Give the position of each P. falciparum parasite with its life-cycle stage, each leukocyte, and any debris.
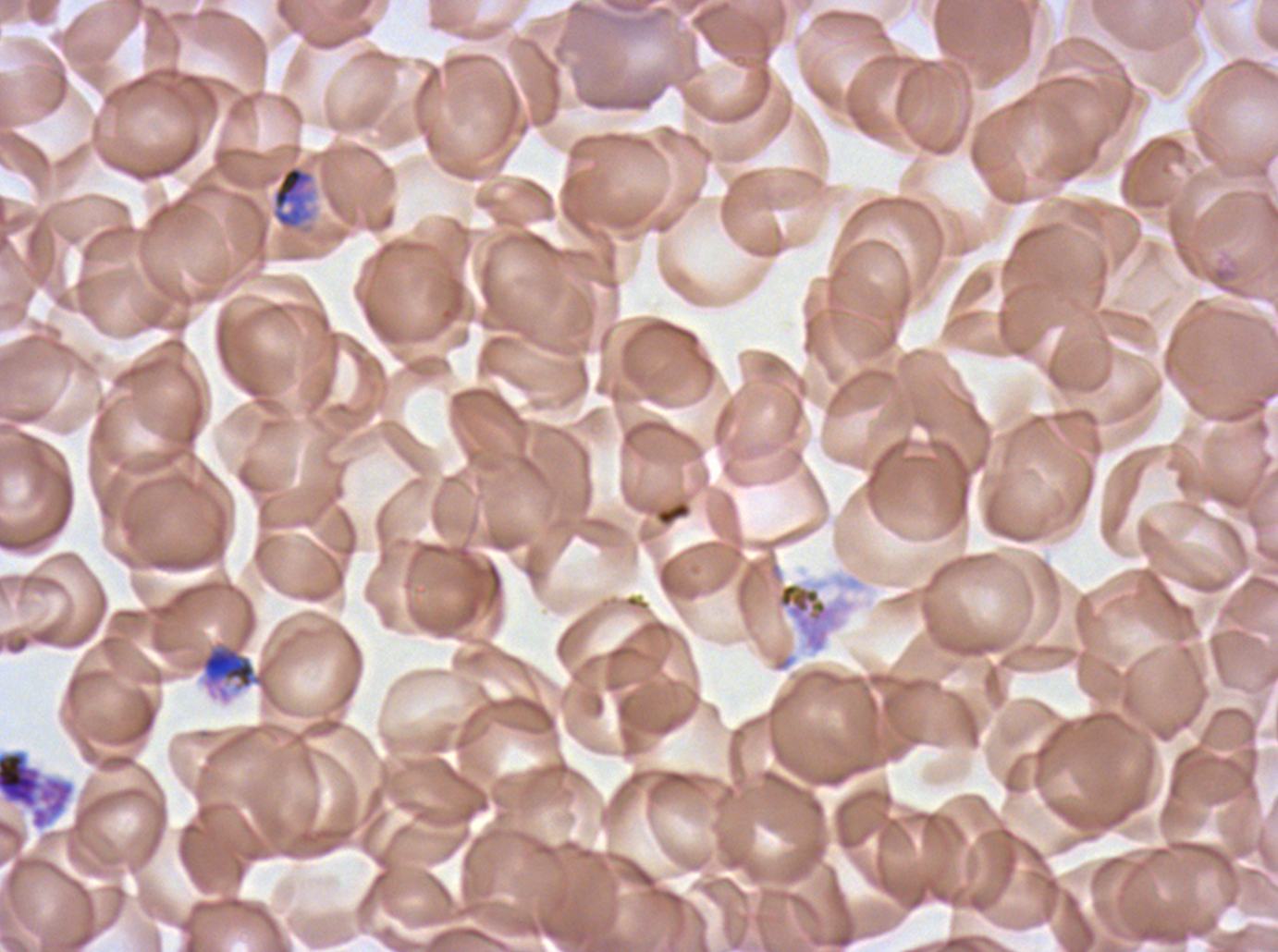

Approximate bounding boxes as [x1, y1, x2, y2] in pixels.
Late trophozoites: [270, 164, 315, 231].
Segmenters: [775, 581, 835, 653], [0, 749, 75, 831].
Debris: [199, 642, 270, 700].
No rings, late-ring/early-trophozoite forms, mid trophozoites, early schizonts, late schizonts, gametocytes, or leukocytes observed.

stain = Giemsa
image size = 1278×952 pixels
specimen = P. falciparum cultured ex vivo for 24 to 48 hours, from a patient in The Gambia
field of view = sub-image separated from a larger composite
life-cycle stages observed = late trophozoite, segmenter
preparation = thin blood film